Outline each Plasmodium vivax-infected red blood cell.
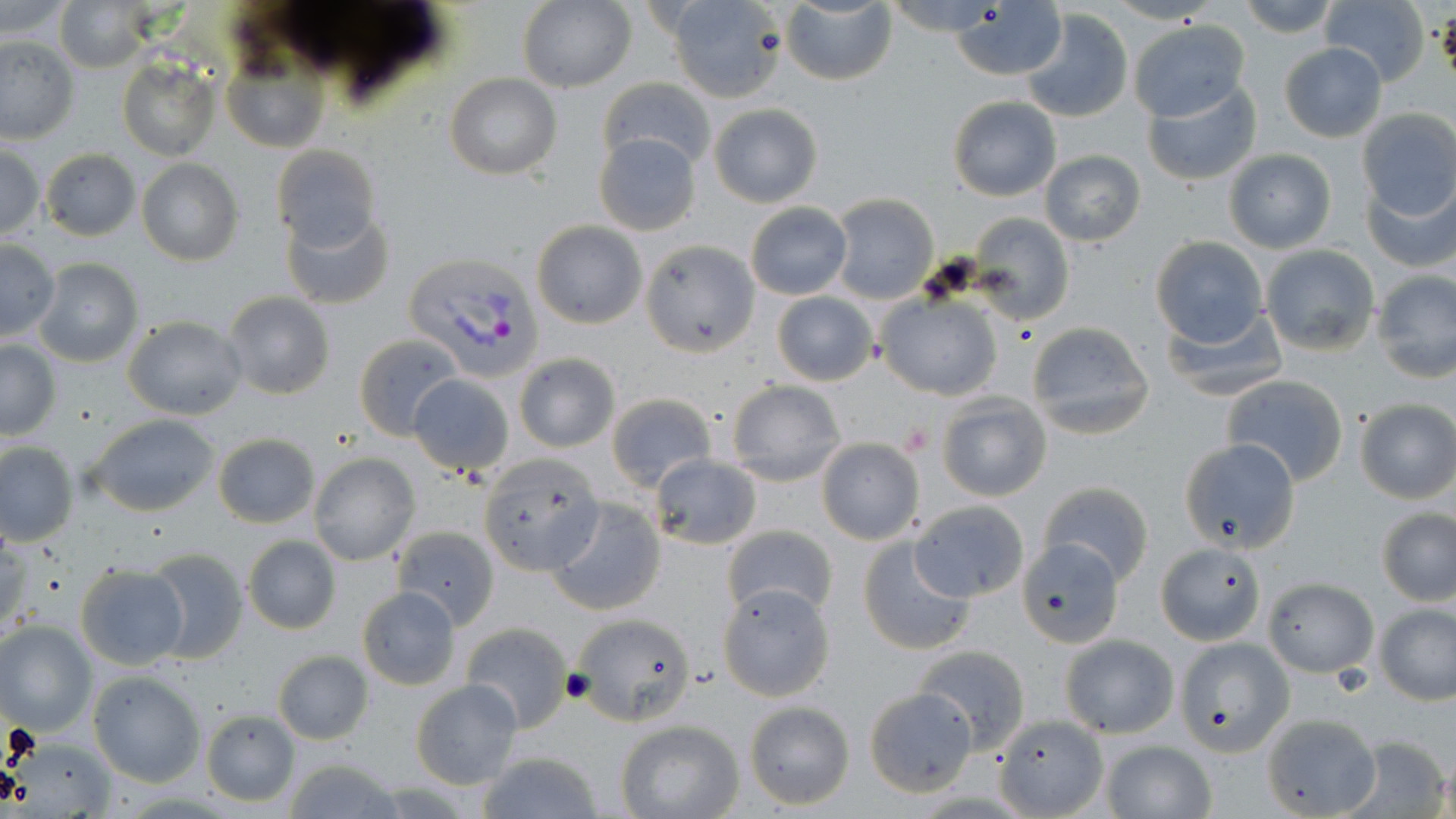

Approximate bounding boxes as [x1, y1, x2, y2] in pixels.
Plasmodium vivax-infected red blood cells: [402, 253, 544, 380].

Uninfected red blood cell locations: [53, 0, 152, 72], [660, 0, 786, 101], [781, 0, 897, 86], [888, 0, 1000, 34], [1232, 0, 1342, 38], [1318, 0, 1431, 87], [1, 1, 75, 40], [517, 1, 636, 93], [950, 1, 1066, 80], [1020, 8, 1134, 123], [1127, 18, 1250, 121], [0, 36, 79, 144], [219, 38, 329, 154], [1278, 42, 1387, 143], [118, 56, 221, 162], [445, 73, 561, 180], [599, 77, 716, 169], [1142, 77, 1262, 186], [947, 95, 1062, 202], [709, 102, 823, 206], [1355, 108, 1456, 222], [594, 132, 700, 236], [0, 143, 46, 242], [271, 144, 382, 255], [41, 148, 140, 240], [1222, 148, 1337, 254], [1039, 150, 1147, 247], [135, 159, 242, 266], [1361, 172, 1456, 273], [830, 194, 938, 303], [745, 202, 851, 300], [282, 206, 395, 310], [966, 213, 1075, 325], [531, 220, 647, 330], [1149, 236, 1268, 348], [1, 239, 58, 343], [643, 240, 760, 356], [1260, 244, 1381, 357], [32, 258, 144, 368], [1371, 270, 1456, 383], [772, 291, 878, 385], [223, 292, 335, 400], [876, 293, 1002, 400], [1161, 305, 1289, 401], [123, 316, 247, 420], [1025, 320, 1154, 439], [353, 333, 464, 440], [0, 339, 60, 442], [514, 353, 622, 454], [408, 374, 514, 476], [1221, 375, 1350, 487], [727, 380, 846, 485], [937, 392, 1051, 501], [606, 393, 718, 490], [1354, 398, 1456, 504], [87, 414, 222, 517], [211, 433, 320, 528], [816, 437, 926, 546], [1179, 438, 1301, 554], [0, 442, 78, 547], [477, 451, 605, 576], [309, 454, 420, 567], [649, 455, 761, 550], [1039, 481, 1154, 585], [545, 496, 668, 616], [910, 502, 1029, 604], [1376, 507, 1456, 607], [723, 524, 837, 620], [391, 526, 498, 629], [857, 534, 976, 656], [242, 536, 341, 636], [1018, 541, 1126, 649], [1156, 542, 1267, 646], [142, 546, 248, 664], [74, 563, 189, 670], [1262, 577, 1379, 676], [720, 583, 833, 702], [357, 587, 461, 689], [1374, 602, 1456, 705], [578, 616, 698, 729], [0, 620, 96, 735], [461, 622, 571, 732], [1058, 635, 1177, 739], [1172, 638, 1291, 754], [913, 646, 1030, 754], [272, 650, 373, 745], [89, 671, 206, 786], [410, 680, 522, 788], [866, 688, 977, 795], [743, 702, 855, 810], [200, 709, 300, 807], [1262, 710, 1384, 815], [993, 715, 1108, 819], [616, 720, 744, 818], [1346, 735, 1450, 818], [1097, 740, 1216, 819], [473, 751, 603, 819], [278, 758, 409, 819]. Platelet locations: [899, 424, 933, 456]. Slide-level diagnosis: Plasmodium vivax. Captured at 1000x magnification. Image is 1456×819 pixels. Thin blood smear. May-Grünwald-Giemsa-stained preparation. Optical microscopy. Single field of view.